State the preparation type.
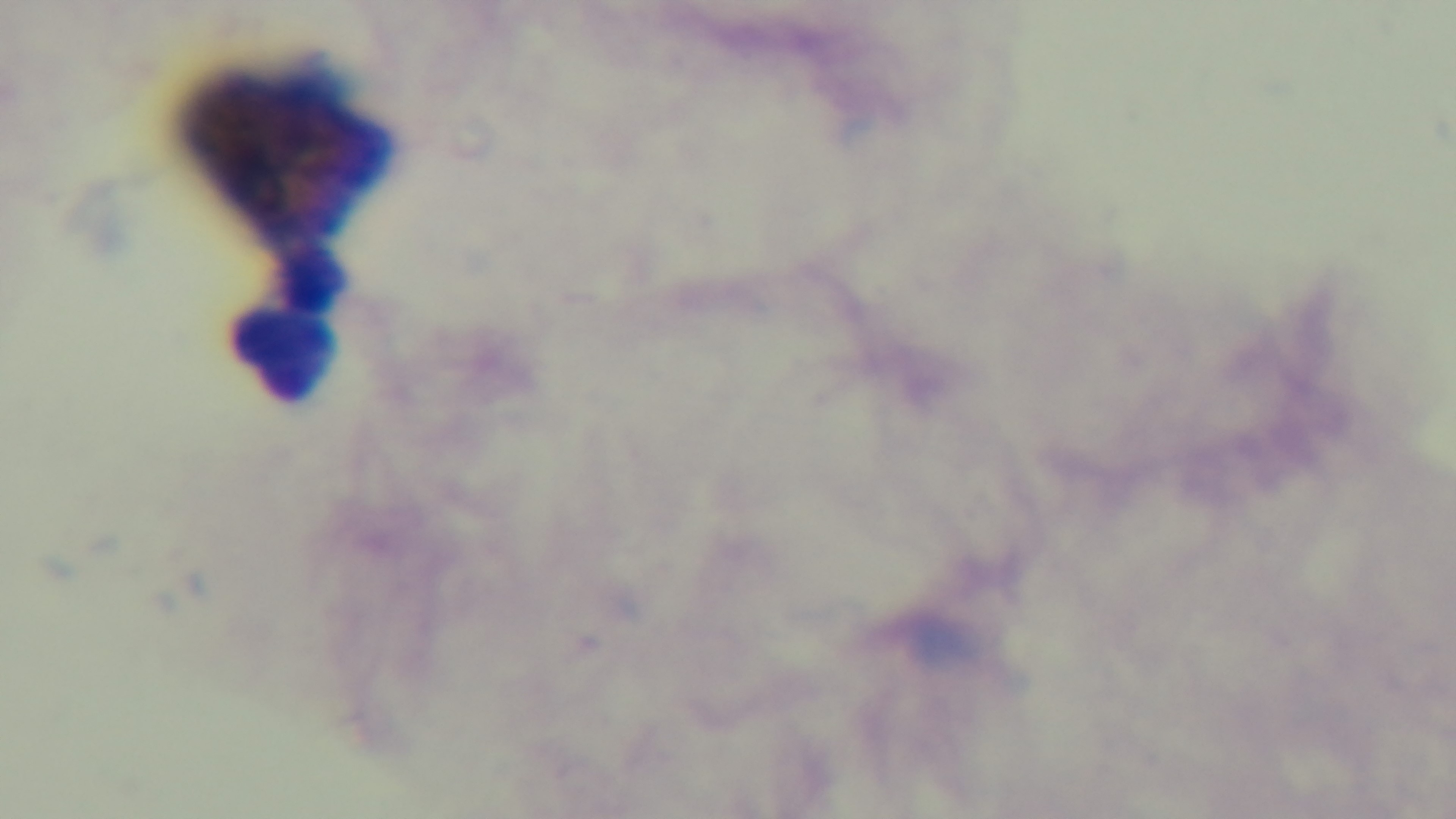

A thick smear.

{
  "modality": "light microscopy",
  "objective": "100x oil immersion",
  "malaria_status": "negative",
  "field_of_view": "one from the slide",
  "stain": "Giemsa",
  "capture": "mounted 4K digital camera"
}